State which parasite is depicted.
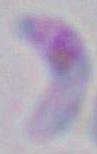

This is Toxoplasma gondii.

Summary:
  - Magnification: 1000x
  - Modality: micrograph